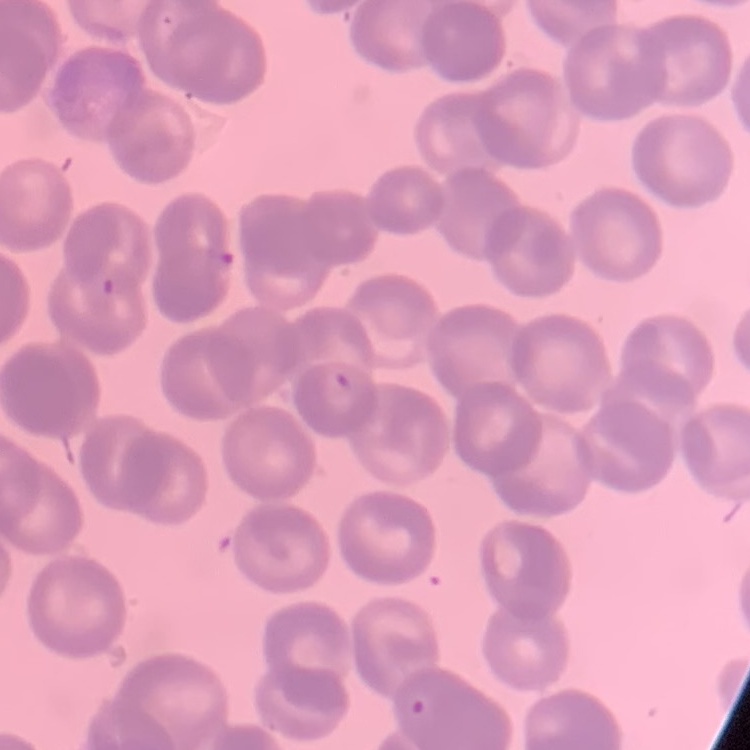

red blood cell morphology = rouleaux formation
preparation = thin peripheral smear
image type = one tile cut from a larger photomicrograph
stain = Field's or Giemsa